Comment on the background quality.
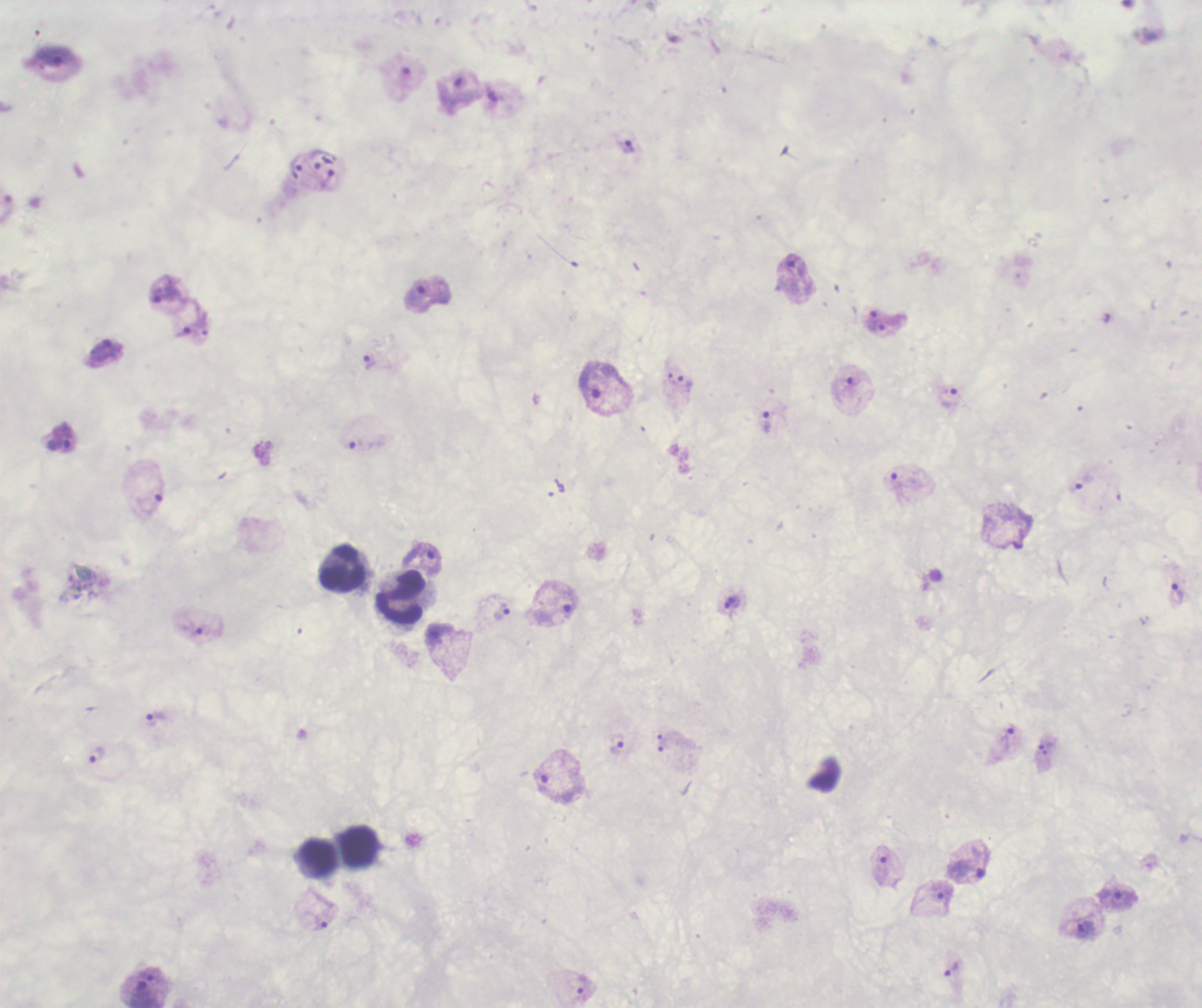

Unsatisfactory.

Approximate centers as (x, y) in pixels. Trophozoite locations: (53, 56), (458, 90), (626, 144), (327, 179), (794, 270), (166, 294), (426, 295), (872, 319), (188, 327), (105, 351), (369, 363), (603, 382), (685, 385), (949, 397), (765, 421), (60, 437), (1078, 484), (429, 559), (1176, 594), (731, 601), (554, 612), (502, 613), (194, 630), (155, 720), (1006, 740), (617, 743), (95, 755), (555, 780), (966, 871), (1118, 897), (1087, 929), (951, 968), (583, 988), (143, 991). Leukocyte locations: (343, 570), (401, 598), (360, 848), (316, 856). Image is 1202×1008 pixels. Thick blood smear. One field from this slide. 100x magnification. Previously used in a real diagnosis. Romanowsky-stained preparation. Result: positive for malaria parasites.